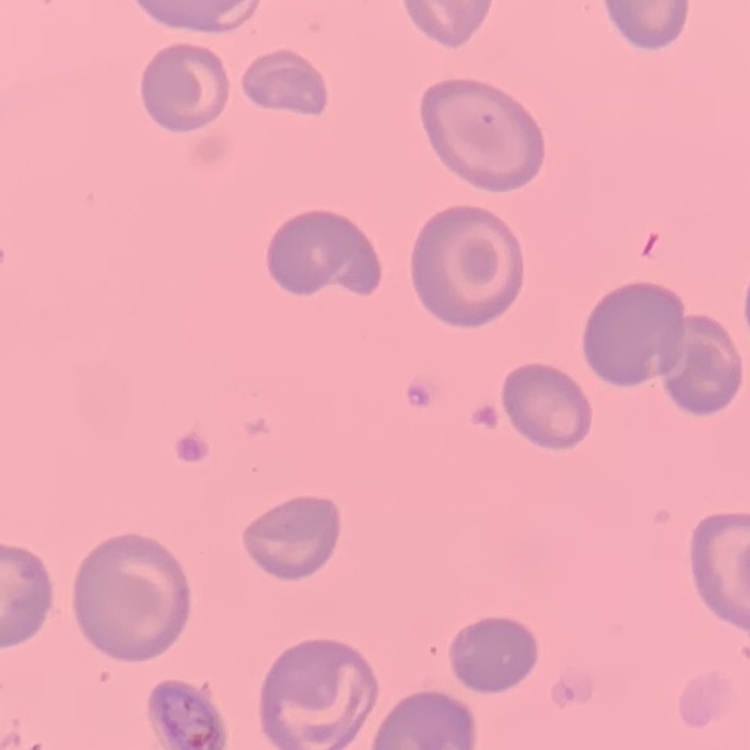
erythrocyte_morphology: no rouleaux formation
preparation: thin peripheral smear
stain: Field's or Giemsa
image_type: square crop of a larger photomicrograph